Report the malaria status of this cell.
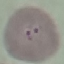

Uninfected.

Summary:
  - Image type: automatically extracted cell patch, resized to 64 × 64 pixels
  - Capture: smartphone camera at the microscope eyepiece
  - Stain: Giemsa
  - Preparation: thin smear